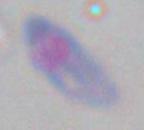

{
  "modality": "micrograph",
  "magnification": "1000x",
  "identification": "Toxoplasma gondii"
}